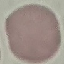
result = no malaria parasites seen
preparation = thin blood film
capture = smartphone through the microscope eyepiece
stain = Giemsa
image type = cell patch, automatically extracted from a larger field of view and resized to 64 × 64 pixels